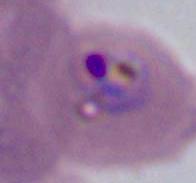

Summary:
  - Magnification: 400x or 1000x
  - Identification: Plasmodium
  - Modality: photomicrograph